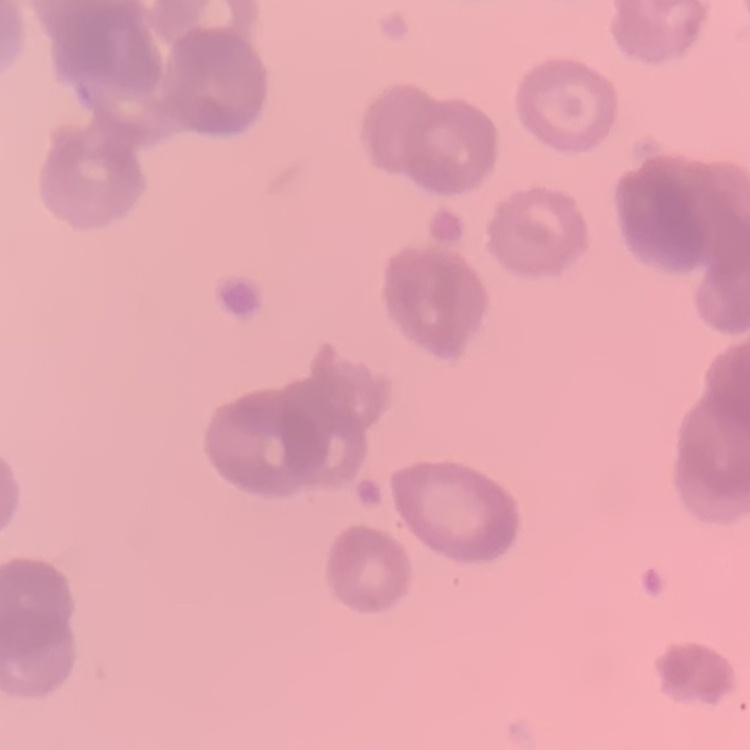
{
  "erythrocyte_morphology": "rouleaux formation",
  "image_type": "square crop of a larger photomicrograph",
  "stain": "Field's or Giemsa",
  "preparation": "thin blood smear"
}